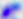
Summary:
  - Magnification: 400x
  - Identification: Toxoplasma gondii
  - Modality: micrograph